Report the malaria status of this cell.
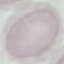
Uninfected.

capture = smartphone through the microscope eyepiece
stain = Giemsa
preparation = thin blood film
image type = cell patch, automatically extracted from a larger field of view and resized to 64 × 64 pixels